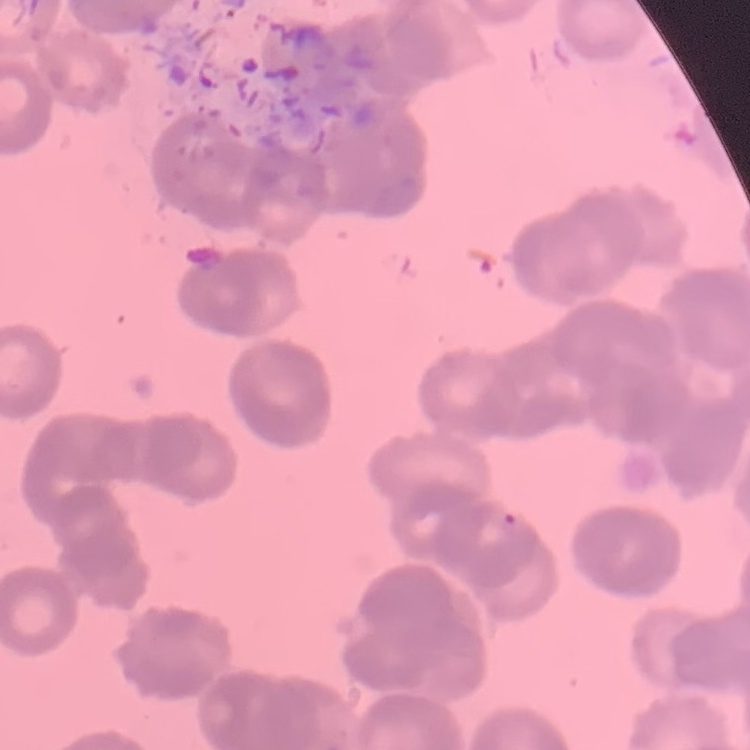

Summary:
  - Red blood cell morphology: rouleaux formation
  - Image type: one tile cut from a larger photomicrograph
  - Preparation: thin blood smear
  - Stain: Field's or Giemsa